Name the parasite shown.
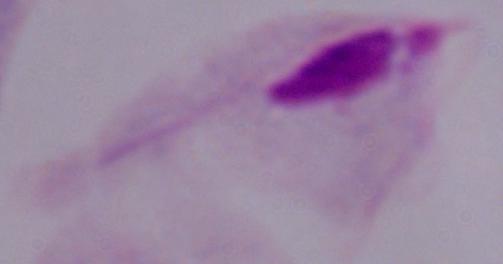

This is a trichomonad.

Micrograph. 1000x magnification.